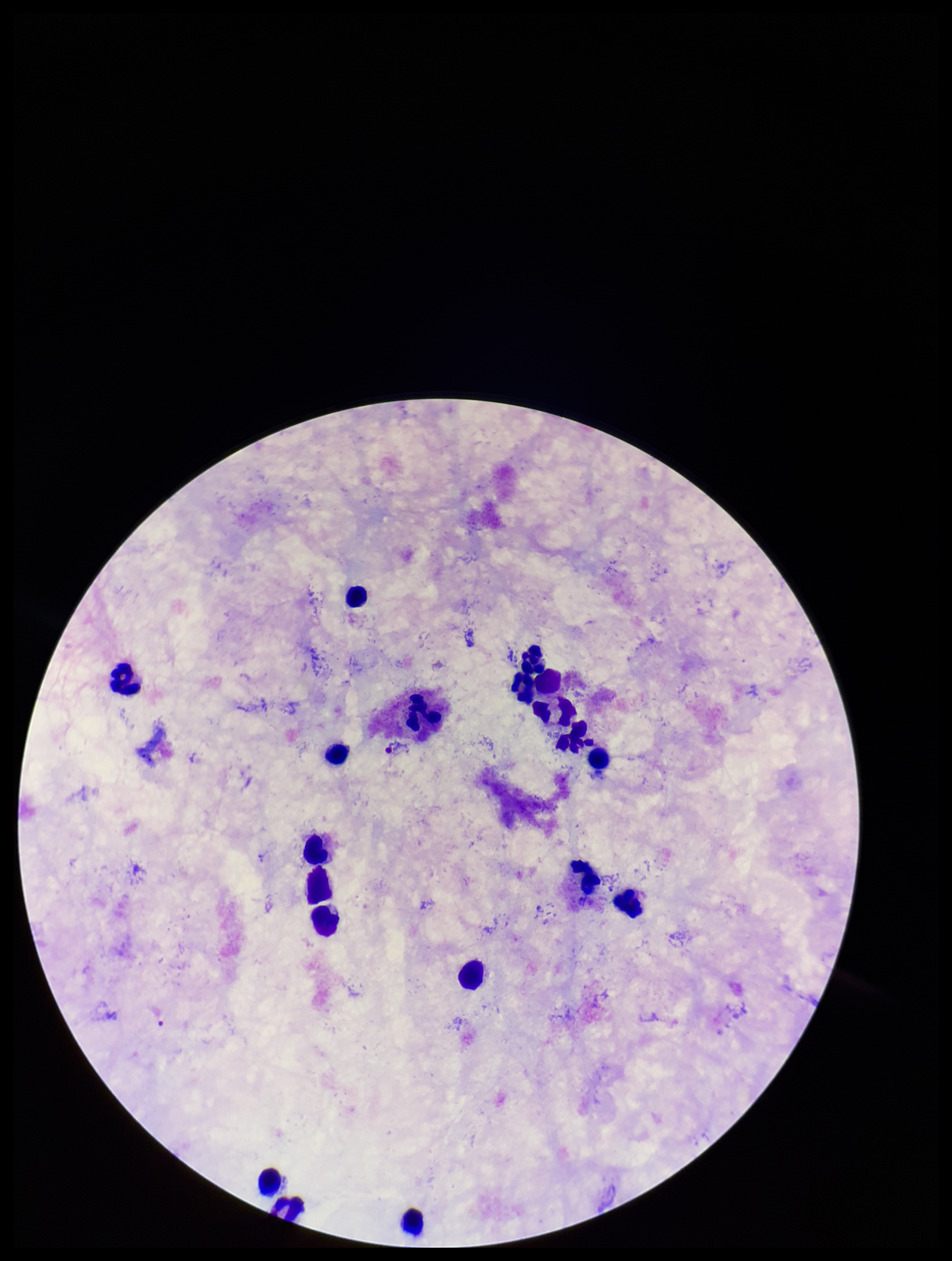

Summary:
  - Image size: 952×1261 pixels
  - Plasmodium parasites: none identified
  - Capture: smartphone photograph through the microscope eyepiece
  - Leukocyte count: 18
  - Field of view: single
  - Patient malaria status: negative
  - Preparation: thick smear
  - Stain: Giemsa
  - Parasite count: 0